State which cell type is depicted.
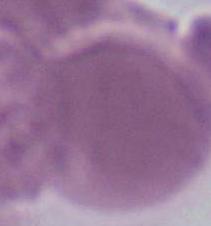
This is an erythrocyte.

{
  "magnification": "1000x",
  "modality": "micrograph"
}